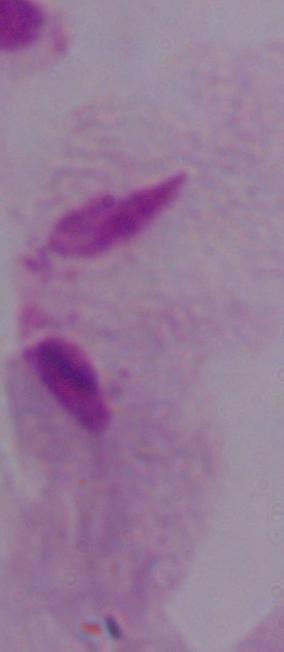

Photomicrograph. Captured at 1000x magnification. A trichomonad is seen.